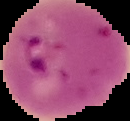 Segmented cell region on a black background. Result: Plasmodium parasites detected. From a thin blood smear. Image is 130×121 pixels.